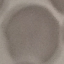

result: negative for malaria parasites
image_type: automatically extracted cell patch, resized to 64 × 64 pixels
capture: smartphone camera at the microscope eyepiece
preparation: thin blood film
stain: Giemsa